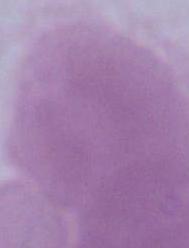
An erythrocyte is shown. Micrograph. 1000x magnification.